Describe the morphology of the red blood cells.
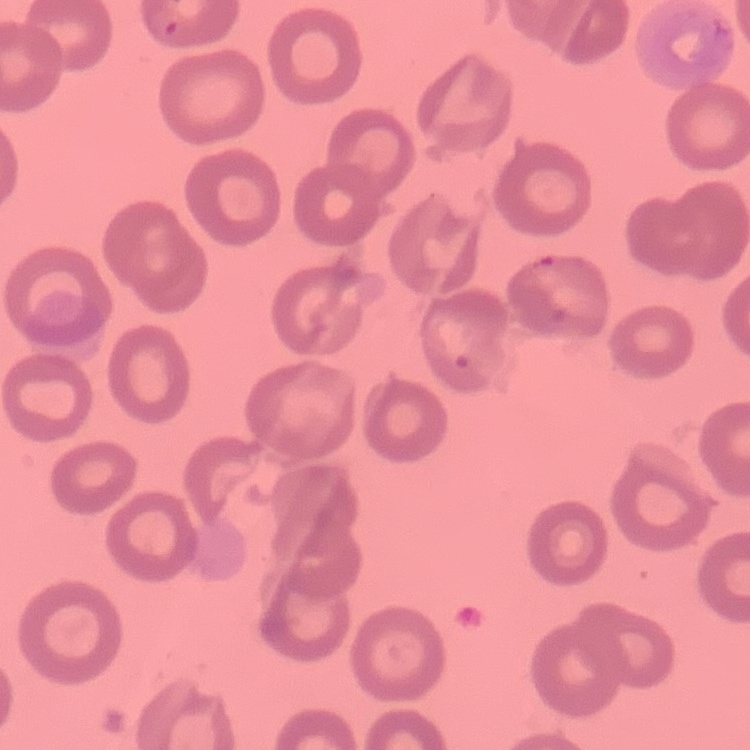
They show no rouleaux formation.

Thin blood smear. Square crop of a larger photomicrograph. Stained with either Field's or Giemsa.